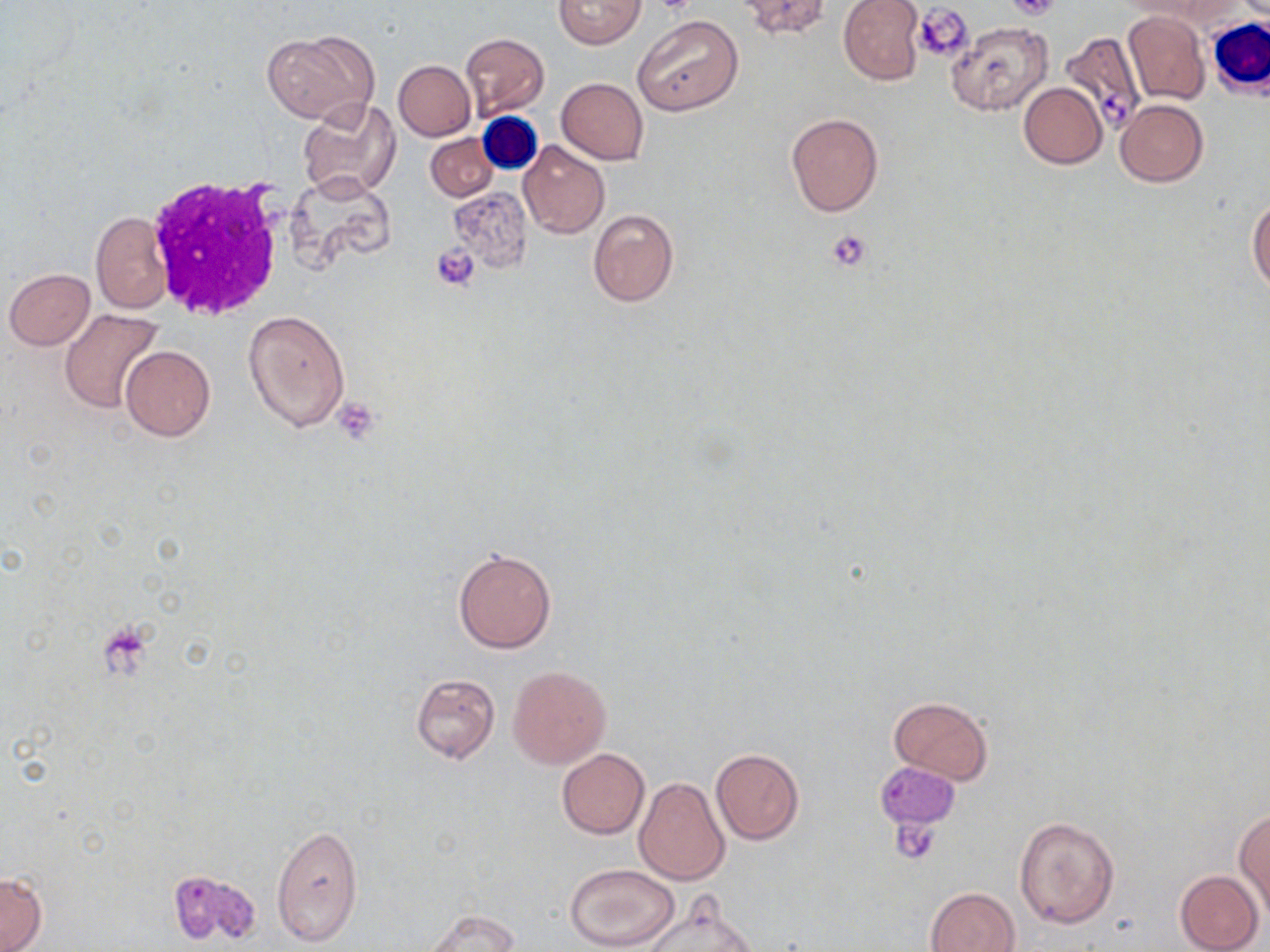

Approximate bounding boxes as (x1,y1)-(x2,y2) corner pairs in pixels. Uninfected red blood cell locations: (553,0)-(645,49), (732,0)-(832,40), (837,0)-(926,86), (1121,11)-(1209,104), (634,15)-(743,117), (948,21)-(1053,117), (261,31)-(377,123), (1058,32)-(1145,127), (460,33)-(549,119), (392,60)-(475,141), (557,78)-(648,164), (1019,83)-(1108,169), (297,97)-(400,202), (1115,100)-(1208,186), (786,112)-(884,216), (425,133)-(499,202), (519,140)-(610,239), (286,169)-(396,273), (448,185)-(532,274), (1247,196)-(1270,296), (587,208)-(678,306), (90,211)-(173,314), (3,268)-(96,350), (59,308)-(164,414), (243,310)-(348,434), (120,345)-(216,441), (452,548)-(556,653), (507,665)-(611,769), (410,672)-(500,763), (888,696)-(993,785), (556,748)-(649,838), (710,749)-(805,845), (633,776)-(731,884), (1235,809)-(1270,913), (1015,816)-(1120,929), (270,823)-(363,947), (564,863)-(679,951), (167,867)-(262,948), (1174,870)-(1264,952), (0,873)-(47,951), (927,887)-(1020,952), (638,892)-(761,952), (425,909)-(520,951). White blood cell locations: (1207,17)-(1270,96), (143,172)-(292,321). Platelet locations: (1006,0)-(1064,22), (914,3)-(974,62), (827,228)-(873,272), (431,242)-(480,290), (333,397)-(383,445), (94,623)-(155,681), (875,763)-(957,832), (889,820)-(942,863). Slide-level diagnosis: negative for blood parasites. One field of a larger specimen. May-Grünwald-Giemsa stain. Captured at 1000x magnification. Thin blood film. Optical microscopy. Image is 1270×952 pixels.